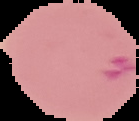
From a thin blood smear. The area outside the segmented cell region is set to black. Result: malaria parasites identified. Image is 139×121 pixels.